Name the blood parasite species.
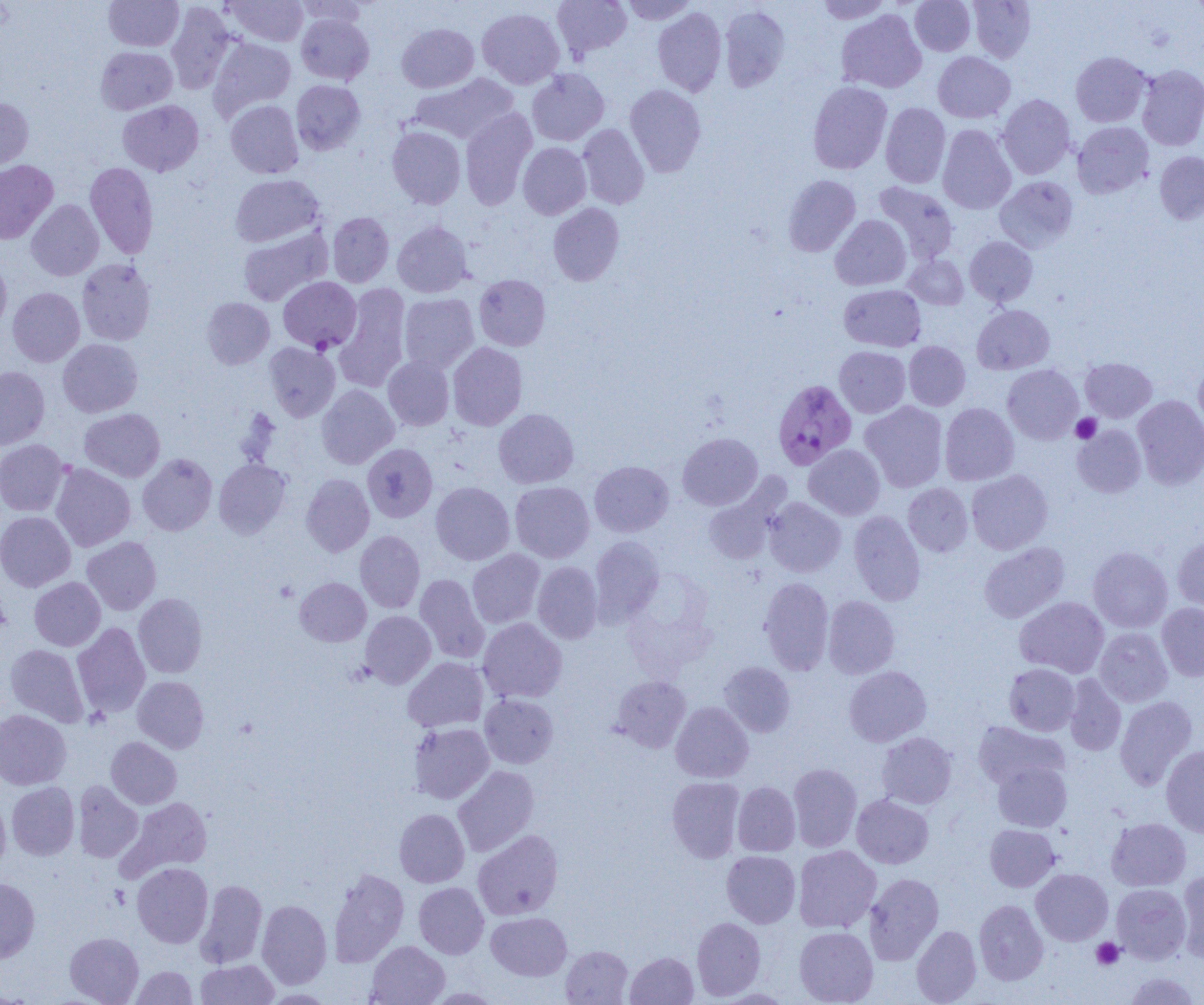

Plasmodium falciparum.

Summary:
  - Coordinate format: approximate bounding boxes as [x1, y1, x2, y2] in pixels
  - Plasmodium falciparum-infected red blood cell locations: [279, 276, 361, 352], [773, 379, 856, 469]
  - Platelet locations: [1071, 413, 1101, 443], [274, 580, 298, 602], [1092, 938, 1124, 969]
  - Uninfected red blood cell locations: [103, 0, 184, 51], [225, 0, 309, 46], [295, 0, 369, 29], [552, 0, 632, 59], [622, 0, 697, 25], [815, 0, 892, 24], [910, 0, 975, 55], [968, 0, 1036, 62], [166, 2, 234, 94], [719, 5, 791, 92], [653, 7, 727, 97], [477, 8, 565, 89], [836, 9, 927, 93], [296, 13, 374, 85], [397, 23, 479, 93], [208, 37, 296, 120], [95, 46, 177, 114], [1070, 51, 1151, 127], [933, 52, 1015, 122], [1136, 65, 1204, 151], [527, 68, 609, 146], [409, 73, 519, 144], [291, 80, 365, 155], [807, 81, 892, 174], [625, 84, 706, 177], [998, 94, 1076, 179], [0, 97, 33, 173], [118, 100, 204, 176], [225, 100, 303, 178], [881, 103, 950, 188], [460, 108, 537, 210], [1072, 121, 1153, 198], [577, 124, 649, 209], [937, 124, 1016, 214], [387, 126, 465, 209], [518, 142, 591, 219], [1154, 150, 1204, 225], [0, 160, 58, 244], [85, 162, 158, 258], [230, 174, 324, 247], [783, 175, 861, 257], [995, 176, 1078, 252], [874, 182, 959, 264], [26, 199, 103, 280], [548, 202, 624, 286], [327, 212, 394, 287], [830, 215, 911, 290], [392, 221, 473, 297], [237, 226, 332, 306], [964, 236, 1038, 306], [905, 254, 968, 309], [0, 257, 11, 336], [77, 259, 156, 345], [474, 275, 551, 351], [335, 284, 410, 393], [839, 284, 926, 352], [8, 287, 84, 367], [399, 293, 479, 373], [201, 297, 275, 369], [972, 305, 1055, 375], [58, 339, 143, 417], [904, 341, 970, 411], [264, 342, 340, 421], [448, 342, 527, 430], [834, 346, 910, 417], [383, 356, 454, 430], [1080, 358, 1156, 422], [1193, 361, 1204, 437], [1002, 365, 1083, 444], [0, 366, 49, 450], [317, 384, 399, 469], [1133, 395, 1204, 490], [860, 401, 948, 492], [940, 403, 1019, 485], [79, 408, 165, 482], [494, 408, 579, 488], [1072, 424, 1147, 497], [677, 432, 762, 510], [0, 439, 68, 516], [362, 443, 437, 522], [804, 444, 885, 520], [137, 453, 217, 536], [214, 459, 291, 538], [589, 461, 673, 537], [51, 463, 135, 551], [966, 470, 1053, 554], [301, 474, 374, 556], [510, 481, 594, 562], [431, 482, 514, 565], [903, 483, 972, 557], [704, 485, 784, 565], [764, 497, 846, 577], [848, 510, 925, 606], [0, 511, 76, 591], [355, 531, 425, 612], [82, 536, 161, 615], [589, 536, 664, 626], [1173, 536, 1204, 613], [979, 542, 1070, 623], [1088, 546, 1173, 632], [467, 549, 545, 628], [532, 562, 603, 644], [415, 574, 489, 664], [29, 577, 105, 651], [295, 577, 371, 647], [759, 577, 833, 675], [133, 593, 207, 678], [823, 596, 899, 678], [1015, 596, 1109, 678], [1157, 603, 1204, 681], [360, 611, 436, 688], [478, 618, 567, 703], [72, 622, 150, 718], [1094, 627, 1173, 706], [5, 644, 89, 727], [403, 657, 488, 732], [718, 661, 796, 737], [1004, 663, 1079, 735], [844, 666, 932, 746], [610, 675, 691, 752], [1064, 675, 1126, 755], [133, 676, 209, 753], [480, 694, 559, 769], [1115, 696, 1198, 790], [670, 702, 753, 782], [0, 709, 71, 790], [973, 721, 1068, 790], [408, 722, 494, 804], [877, 732, 957, 809], [106, 737, 181, 809], [1161, 745, 1204, 836], [992, 760, 1072, 832], [788, 762, 862, 852], [453, 765, 539, 856], [666, 776, 744, 863], [73, 780, 143, 862], [732, 781, 800, 856], [7, 782, 79, 860], [0, 794, 11, 874], [852, 794, 933, 868], [122, 796, 213, 878], [394, 808, 469, 887], [1107, 817, 1191, 891], [985, 824, 1060, 892], [473, 829, 563, 920], [793, 845, 881, 933], [721, 850, 800, 927], [132, 862, 213, 947], [328, 868, 409, 967], [1031, 868, 1113, 945], [1177, 869, 1204, 962], [864, 873, 944, 965], [0, 877, 40, 963], [1031, 877, 1191, 952], [196, 879, 267, 968], [414, 882, 489, 958], [1111, 884, 1191, 964], [257, 899, 332, 988], [974, 900, 1048, 985], [486, 912, 571, 981], [691, 917, 765, 1000], [911, 925, 982, 1004], [794, 927, 877, 1005], [65, 932, 144, 1004], [366, 940, 449, 1005], [561, 945, 633, 1004], [625, 951, 698, 1004], [195, 959, 279, 1005], [131, 966, 198, 1004], [1124, 971, 1200, 1005]
  - Modality: light microscopy
  - Magnification: 1000x
  - Preparation: thin blood film
  - Image size: 1204×1005 pixels
  - Field of view: one of a larger specimen